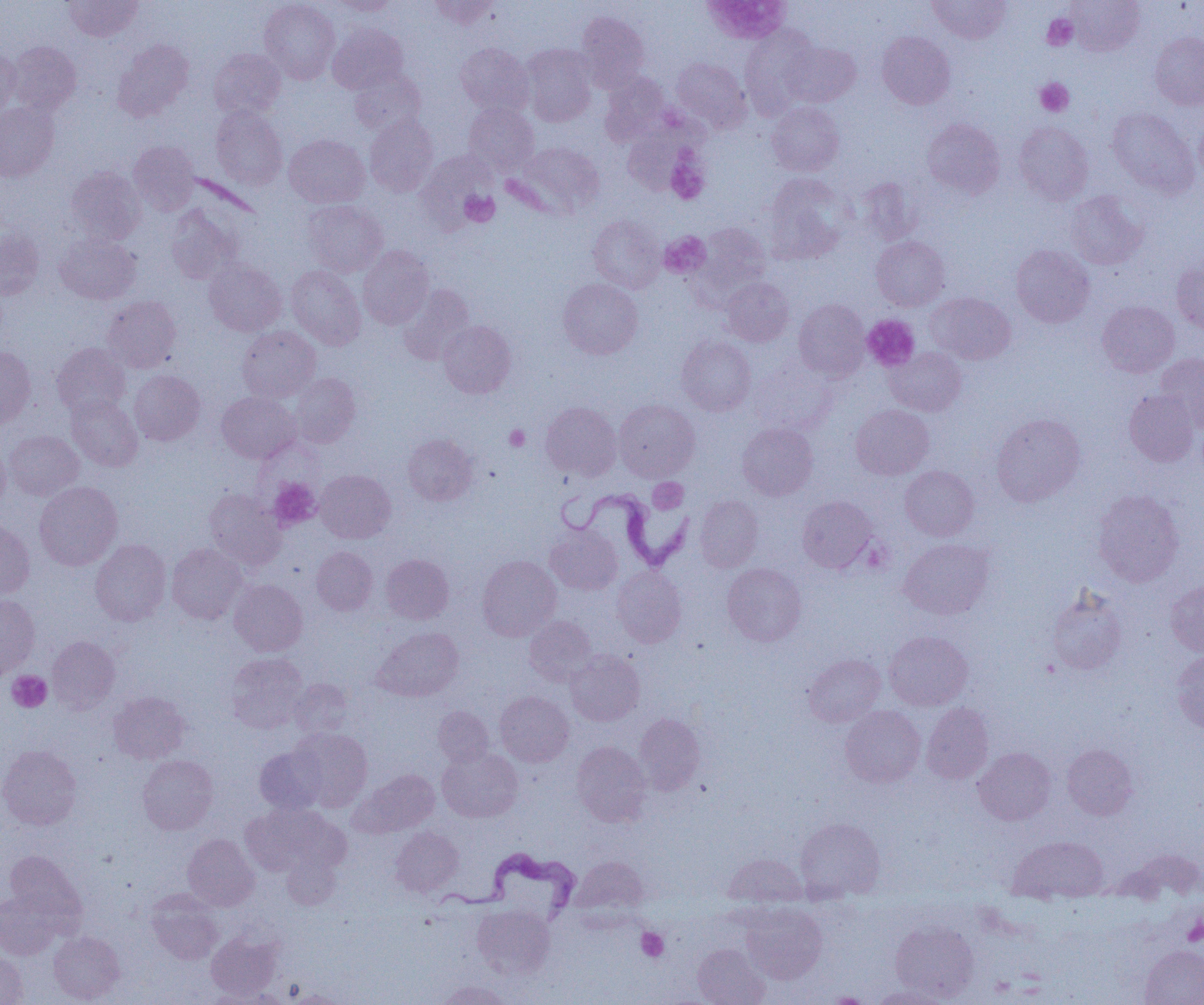
Approximate bounding boxes as (x1, y1, x2, y2) in pixels. Uninfected red blood cell locations: (64, 0, 142, 41), (260, 0, 340, 83), (430, 0, 498, 30), (928, 0, 1011, 43), (1066, 0, 1144, 55), (332, 1, 398, 16), (575, 11, 649, 90), (328, 24, 407, 94), (740, 27, 817, 117), (877, 31, 955, 109), (1149, 32, 1204, 109), (113, 39, 193, 121), (9, 41, 81, 115), (782, 41, 860, 106), (456, 43, 533, 115), (521, 44, 596, 126), (0, 47, 20, 116), (209, 48, 286, 119), (671, 57, 751, 132), (349, 68, 425, 135), (601, 71, 669, 144), (767, 102, 844, 176), (0, 103, 59, 180), (464, 104, 538, 175), (211, 106, 287, 189), (1107, 107, 1198, 198), (1195, 110, 1204, 185), (364, 116, 438, 196), (922, 119, 1005, 198), (1014, 122, 1093, 205), (623, 124, 698, 195), (284, 134, 369, 207), (129, 141, 199, 214), (514, 142, 605, 217), (66, 166, 145, 244), (763, 174, 850, 264), (858, 178, 922, 244), (1066, 191, 1147, 269), (302, 200, 387, 276), (166, 206, 241, 284), (588, 215, 665, 292), (693, 223, 771, 299), (0, 229, 44, 299), (55, 233, 141, 304), (871, 236, 950, 310), (1011, 245, 1094, 327), (358, 246, 434, 329), (204, 258, 286, 336), (1172, 261, 1204, 335), (286, 265, 366, 349), (721, 277, 794, 346), (558, 278, 643, 359), (399, 285, 474, 364), (926, 292, 1015, 364), (102, 296, 181, 372), (793, 300, 869, 380), (1097, 301, 1179, 377), (438, 321, 516, 398), (238, 326, 320, 401), (677, 335, 756, 415), (51, 343, 130, 417), (0, 347, 35, 428), (885, 347, 967, 416), (1157, 353, 1204, 432), (747, 359, 837, 436), (130, 371, 204, 445), (290, 373, 360, 447), (1124, 389, 1200, 467), (217, 392, 300, 463), (66, 395, 143, 471), (614, 399, 699, 482), (541, 402, 621, 480), (851, 405, 934, 479), (991, 413, 1085, 506), (737, 422, 818, 500), (4, 430, 84, 500), (403, 434, 478, 506), (0, 444, 9, 511), (900, 465, 979, 540), (316, 470, 395, 543), (34, 481, 122, 570), (204, 489, 285, 571), (1093, 489, 1184, 587), (695, 495, 763, 572), (797, 496, 878, 573), (0, 520, 34, 599), (545, 524, 622, 595), (899, 538, 993, 619), (90, 539, 171, 625), (167, 543, 247, 623), (311, 546, 378, 615), (381, 554, 453, 624), (477, 555, 561, 640), (722, 563, 806, 647), (612, 567, 686, 648), (229, 579, 307, 656), (1165, 580, 1204, 656), (1047, 586, 1127, 675), (0, 596, 40, 677), (525, 616, 597, 686), (373, 627, 464, 701), (884, 631, 973, 710), (47, 636, 120, 711), (1172, 650, 1204, 735), (566, 651, 645, 726), (226, 653, 308, 733), (803, 654, 885, 727), (291, 678, 354, 738), (109, 691, 190, 763), (495, 691, 574, 766), (922, 703, 993, 784), (433, 706, 493, 766), (840, 706, 926, 787), (634, 713, 705, 794), (290, 727, 373, 811), (571, 741, 652, 827), (1062, 744, 1138, 820), (0, 745, 82, 830), (254, 746, 327, 815), (974, 747, 1056, 825), (438, 748, 522, 823), (137, 754, 218, 834), (353, 769, 440, 837), (240, 804, 343, 877), (795, 817, 886, 901), (390, 827, 463, 896), (182, 834, 259, 910), (1008, 835, 1108, 900), (1123, 849, 1204, 901), (4, 850, 85, 926), (282, 851, 341, 910), (724, 853, 807, 907), (571, 857, 649, 917), (146, 890, 224, 964), (0, 891, 61, 959), (741, 903, 827, 983), (472, 904, 554, 979), (891, 920, 978, 1001), (206, 930, 282, 999), (49, 931, 124, 1003), (692, 942, 770, 1005), (1140, 945, 1204, 1005), (0, 952, 28, 1005), (434, 980, 514, 1005), (868, 985, 951, 1005), (205, 986, 291, 1004), (281, 990, 350, 1004). Trypanosoma brucei locations: (556, 486, 696, 571), (434, 848, 583, 927). Platelet locations: (700, 0, 792, 43), (1043, 14, 1077, 50), (1035, 78, 1074, 116), (666, 158, 709, 204), (460, 190, 499, 226), (659, 232, 710, 278), (862, 315, 919, 371), (505, 425, 530, 451), (268, 477, 321, 530), (648, 478, 687, 513), (7, 671, 51, 712), (1183, 916, 1204, 946), (636, 928, 668, 962). Slide-level diagnosis: Trypanosoma brucei. Image is 1204×1005 pixels. Thin blood smear. Optical microscopy. Single field of view. Captured at 1000x magnification.